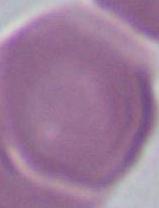
Summary:
  - Identification: red blood cell
  - Magnification: 1000x
  - Modality: micrograph